Outline each Plasmodium falciparum-infected red blood cell.
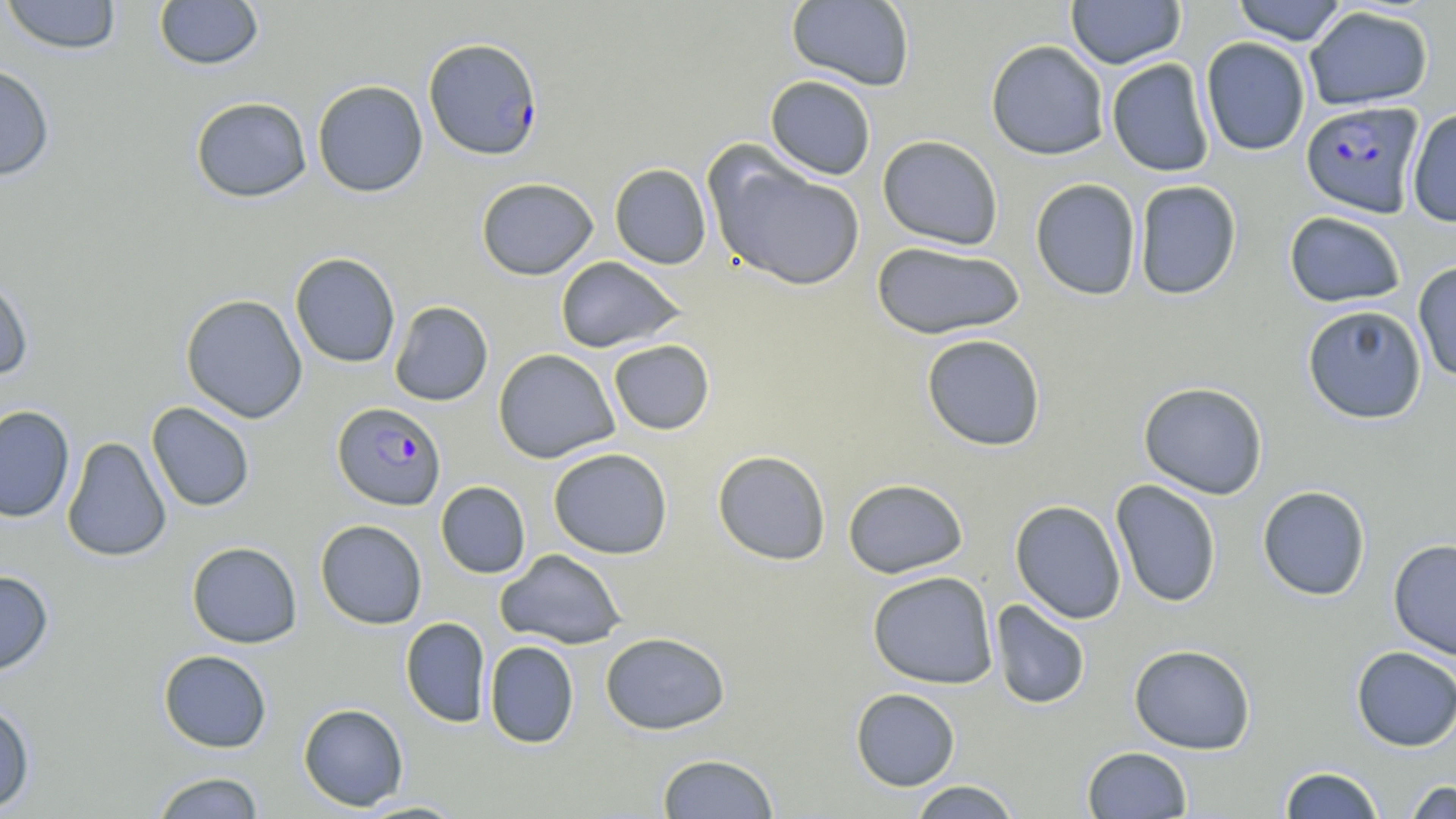

Approximate bounding boxes as named x1/y1/x2/y2 corners in pixels.
Plasmodium falciparum-infected red blood cells: (x1=423, y1=37, x2=543, y2=160), (x1=1300, y1=100, x2=1425, y2=217), (x1=332, y1=402, x2=447, y2=511).

Summary:
  - Uninfected red blood cell locations: (x1=0, y1=0, x2=123, y2=55), (x1=153, y1=0, x2=264, y2=71), (x1=1066, y1=0, x2=1185, y2=69), (x1=1231, y1=0, x2=1348, y2=45), (x1=786, y1=1, x2=916, y2=92), (x1=1304, y1=5, x2=1434, y2=111), (x1=1200, y1=37, x2=1310, y2=156), (x1=985, y1=40, x2=1110, y2=160), (x1=1106, y1=58, x2=1215, y2=177), (x1=0, y1=63, x2=55, y2=181), (x1=765, y1=75, x2=876, y2=180), (x1=312, y1=80, x2=428, y2=197), (x1=190, y1=96, x2=312, y2=202), (x1=1406, y1=108, x2=1456, y2=227), (x1=877, y1=135, x2=1004, y2=250), (x1=707, y1=152, x2=866, y2=292), (x1=609, y1=163, x2=712, y2=269), (x1=476, y1=177, x2=598, y2=280), (x1=1029, y1=178, x2=1142, y2=300), (x1=1132, y1=180, x2=1242, y2=300), (x1=1284, y1=211, x2=1406, y2=308), (x1=871, y1=241, x2=1025, y2=340), (x1=290, y1=252, x2=401, y2=368), (x1=554, y1=256, x2=687, y2=353), (x1=1412, y1=261, x2=1456, y2=382), (x1=0, y1=273, x2=35, y2=382), (x1=180, y1=293, x2=308, y2=423), (x1=389, y1=301, x2=493, y2=406), (x1=1301, y1=304, x2=1428, y2=424), (x1=921, y1=334, x2=1046, y2=451), (x1=608, y1=339, x2=715, y2=435), (x1=493, y1=348, x2=619, y2=463), (x1=1138, y1=381, x2=1268, y2=500), (x1=146, y1=402, x2=255, y2=512), (x1=0, y1=405, x2=75, y2=523), (x1=62, y1=436, x2=172, y2=562), (x1=548, y1=447, x2=673, y2=559), (x1=712, y1=449, x2=831, y2=566), (x1=842, y1=478, x2=969, y2=579), (x1=1110, y1=480, x2=1222, y2=608), (x1=435, y1=481, x2=531, y2=579), (x1=1257, y1=485, x2=1371, y2=601), (x1=1009, y1=500, x2=1127, y2=624), (x1=315, y1=519, x2=428, y2=629), (x1=1388, y1=538, x2=1456, y2=661), (x1=187, y1=541, x2=302, y2=648), (x1=496, y1=548, x2=626, y2=649), (x1=0, y1=569, x2=54, y2=676), (x1=867, y1=571, x2=999, y2=689), (x1=990, y1=599, x2=1091, y2=710), (x1=400, y1=617, x2=491, y2=728), (x1=600, y1=631, x2=730, y2=735), (x1=484, y1=641, x2=580, y2=748), (x1=1128, y1=643, x2=1256, y2=754), (x1=1350, y1=646, x2=1456, y2=751), (x1=158, y1=649, x2=272, y2=753), (x1=850, y1=688, x2=961, y2=791), (x1=0, y1=700, x2=35, y2=814), (x1=298, y1=703, x2=409, y2=811), (x1=1082, y1=746, x2=1193, y2=818), (x1=656, y1=752, x2=780, y2=818), (x1=1279, y1=766, x2=1385, y2=819), (x1=149, y1=771, x2=267, y2=818), (x1=908, y1=780, x2=1022, y2=818), (x1=1403, y1=780, x2=1456, y2=819), (x1=353, y1=799, x2=470, y2=818)
  - Slide-level diagnosis: Plasmodium falciparum
  - Magnification: 1000x
  - Stain: May-Grünwald-Giemsa
  - Preparation: thin blood film
  - Image size: 1456×819 pixels
  - Field of view: single
  - Modality: optical microscopy